Comment on the morphology of the erythrocytes.
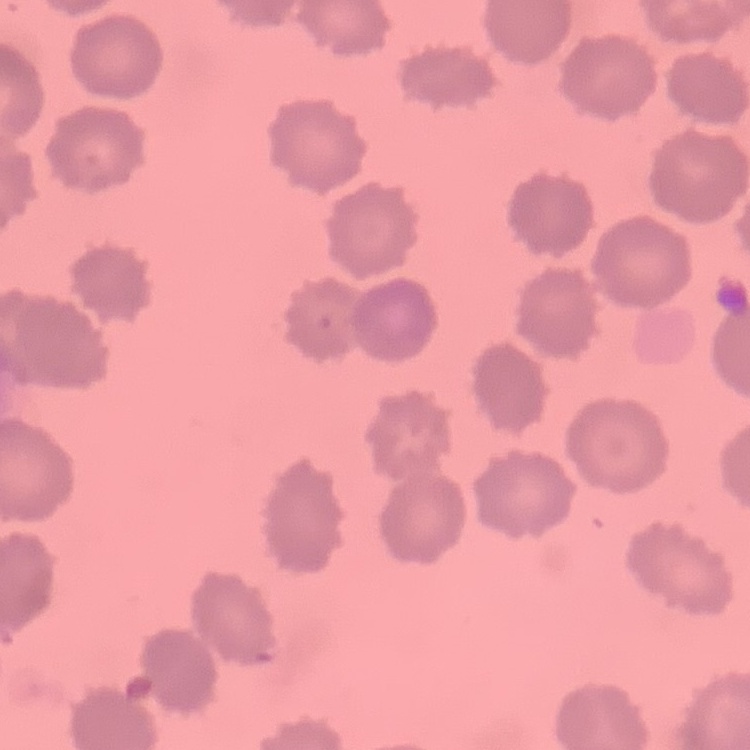

They show no rouleaux formation.

Summary:
  - Image type: one tile cut from a larger photomicrograph
  - Preparation: thin blood film
  - Stain: Field's or Giemsa